Outline each blood parasite and name the species.
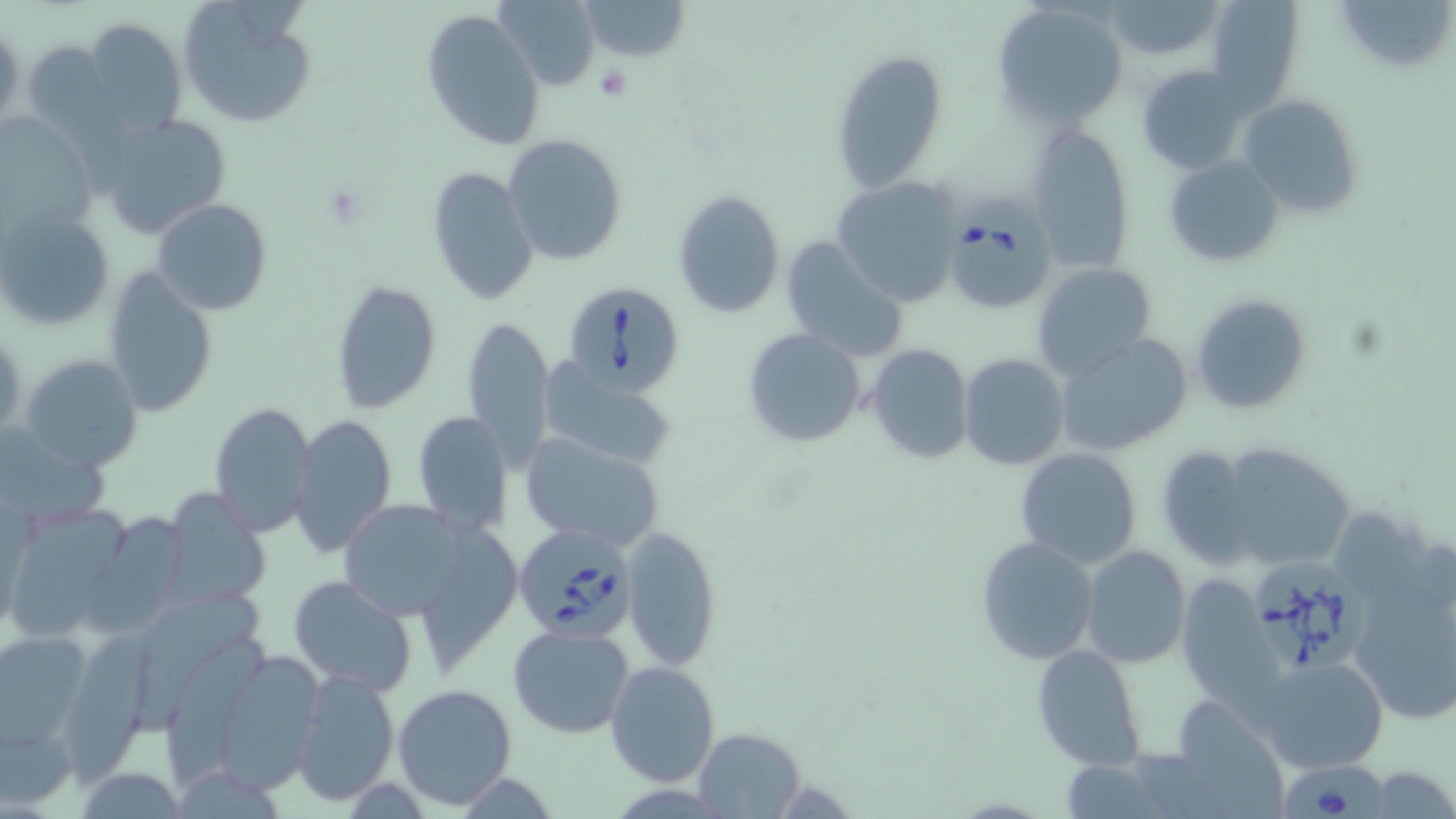
Approximate bounding boxes as (x1,y1)-(x2,y2) corner pairs in pixels.
Babesia divergens-infected red blood cells: (944,194)-(1056,314), (561,279)-(687,397), (515,521)-(637,640), (1247,556)-(1375,681), (1275,760)-(1392,817).
No Plasmodium falciparum, Plasmodium ovale, Plasmodium malariae, Plasmodium vivax, or Trypanosoma brucei observed.

Platelet locations: (595,65)-(631,101). Uninfected red blood cell locations: (496,0)-(600,86), (574,0)-(690,63), (1206,0)-(1303,108), (1334,0)-(1456,76), (1101,1)-(1225,61), (176,2)-(317,130), (994,2)-(1129,128), (422,8)-(544,150), (80,19)-(189,139), (1,24)-(24,133), (20,39)-(119,142), (831,50)-(949,191), (1137,64)-(1250,175), (1237,93)-(1364,221), (0,112)-(100,241), (97,112)-(233,237), (1026,121)-(1137,273), (504,134)-(629,266), (1164,155)-(1286,266), (428,166)-(537,305), (832,177)-(962,307), (673,190)-(785,318), (151,199)-(272,315), (2,210)-(116,336), (779,235)-(910,360), (1032,261)-(1160,378), (102,265)-(218,418), (331,279)-(441,417), (1191,293)-(1313,416), (463,314)-(555,470), (1,326)-(25,441), (741,326)-(867,449), (1053,334)-(1194,457), (865,343)-(973,464), (19,353)-(144,473), (958,353)-(1069,472), (540,368)-(677,471), (210,401)-(316,534), (411,410)-(514,535), (291,414)-(396,556), (518,432)-(666,552), (1217,441)-(1355,570), (1153,444)-(1261,568), (1015,447)-(1144,569), (161,489)-(271,608), (336,500)-(480,621), (12,505)-(138,636), (85,515)-(189,644), (621,526)-(721,672), (975,535)-(1102,666), (1080,546)-(1190,667), (1344,547)-(1455,730), (287,575)-(417,696), (1174,575)-(1278,708), (133,592)-(268,737), (507,624)-(635,738), (65,626)-(161,789), (0,631)-(92,745), (168,634)-(271,782), (1031,644)-(1146,771), (212,649)-(330,790), (1256,655)-(1390,774), (606,662)-(719,786), (292,667)-(398,805), (392,684)-(518,810), (1169,697)-(1287,817), (2,716)-(75,809), (692,729)-(805,817), (72,765)-(187,818), (1368,766)-(1456,819). Slide-level diagnosis: Babesia divergens. Image is 1456×819 pixels. May-Grünwald-Giemsa-stained preparation. Single field of view. Thin blood film. Light microscopy. 1000x magnification.